Comment on the morphology of the erythrocytes.
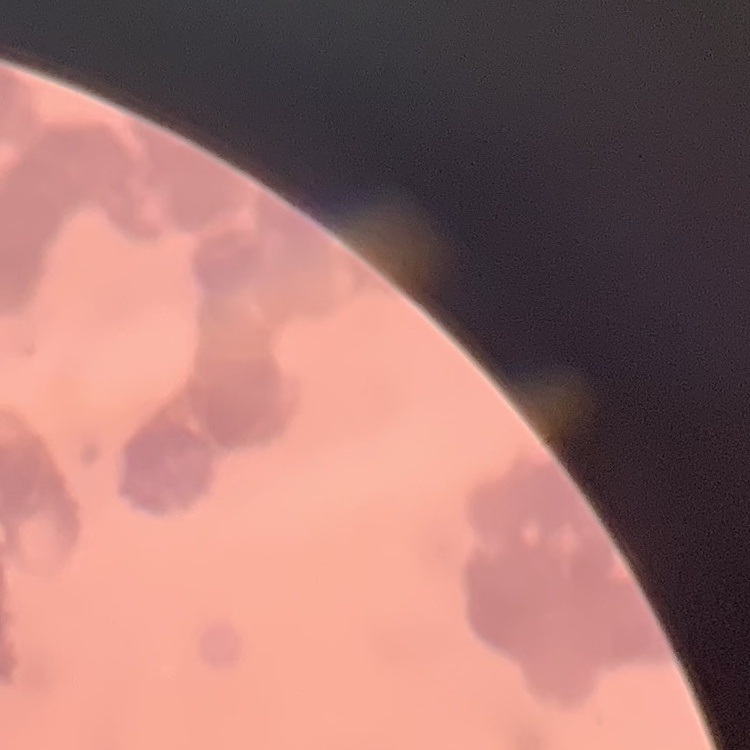
Rouleaux formation.

stain: Field's or Giemsa
image_type: one tile cut from a larger photomicrograph
preparation: thin blood film